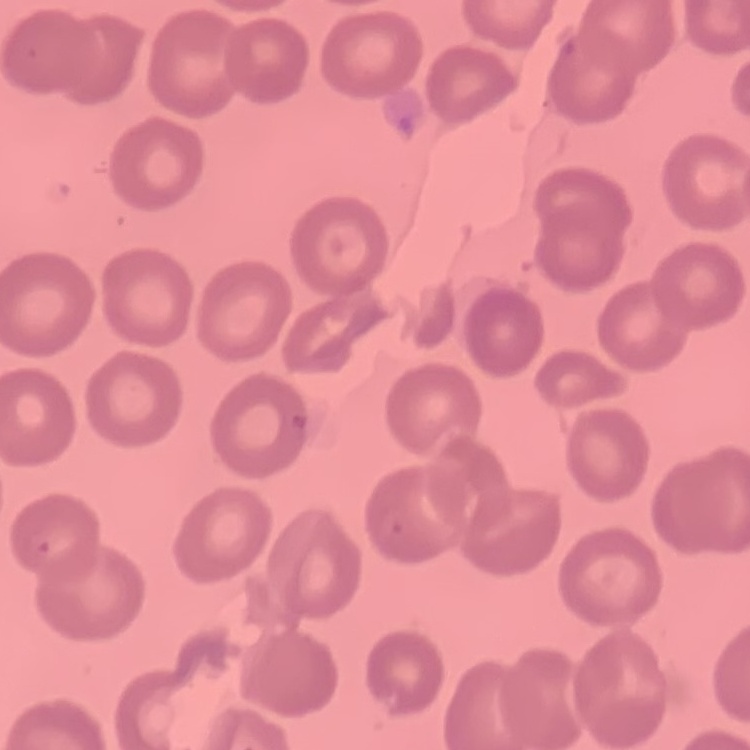
{
  "red_blood_cell_morphology": "no rouleaux formation",
  "image_type": "one tile cut from a larger photomicrograph",
  "stain": "Field's or Giemsa",
  "preparation": "thin blood smear"
}